Classify this cell by malaria status.
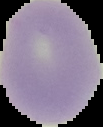

Uninfected.

Summary:
  - Image size: 103×127 pixels
  - Preparation: thin blood smear
  - Image type: cell region segmented out of the field of view; surrounding area masked to black